Outline each blood parasite and name the species.
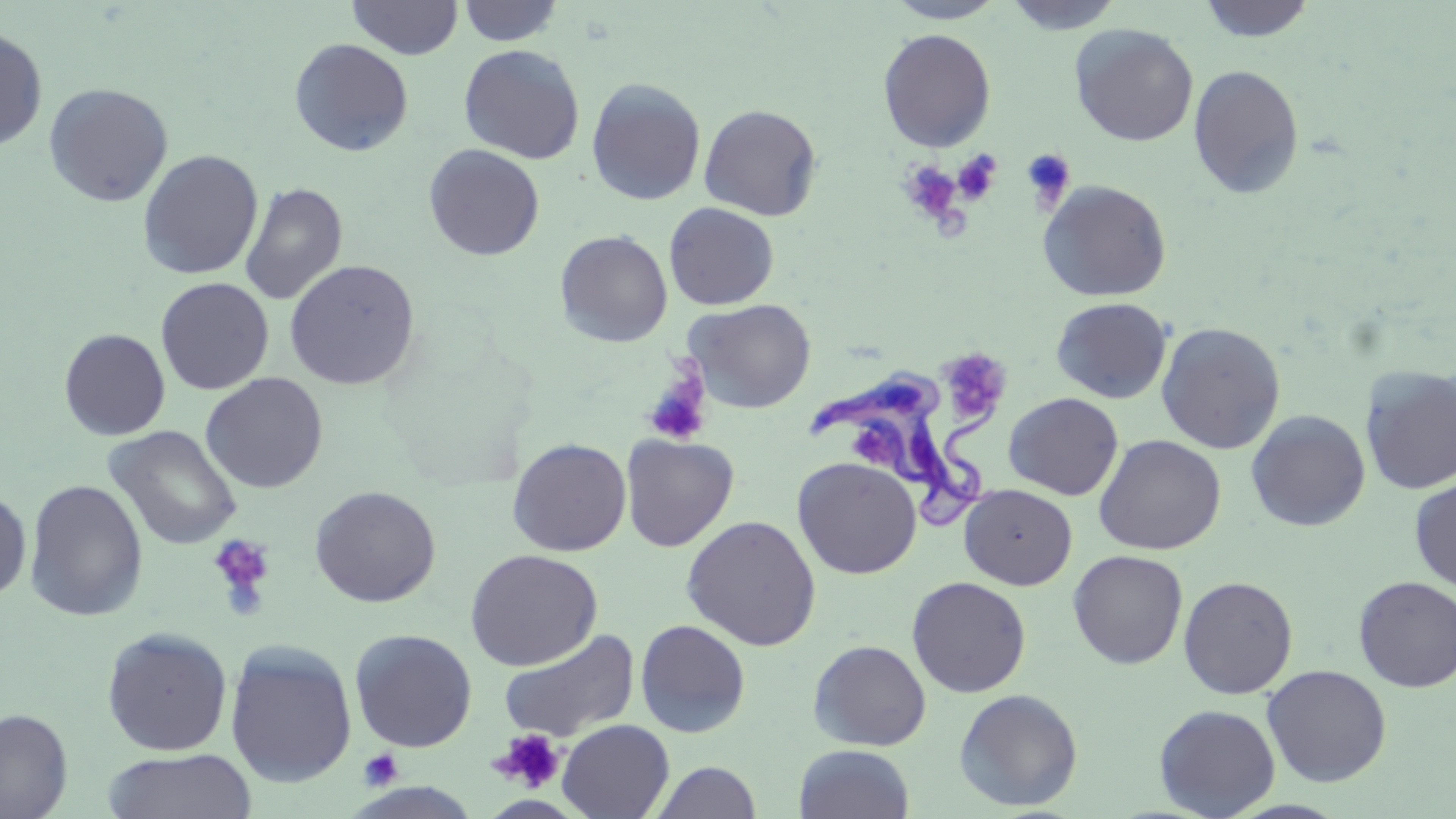

Approximate bounding boxes as [x1, y1, x2, y2] in pixels.
Trypanosoma brucei: [806, 366, 1003, 533].
No Plasmodium falciparum, Plasmodium ovale, Plasmodium malariae, Plasmodium vivax, or Babesia divergens observed.

Uninfected red blood cell locations: [348, 0, 462, 60], [885, 0, 1007, 24], [1002, 0, 1127, 35], [1197, 0, 1316, 42], [457, 1, 563, 46], [1069, 24, 1198, 147], [0, 25, 48, 151], [877, 28, 996, 153], [288, 38, 414, 157], [458, 44, 585, 165], [1188, 64, 1304, 200], [586, 78, 706, 206], [43, 82, 173, 207], [699, 103, 823, 221], [423, 144, 545, 261], [137, 150, 263, 280], [1037, 179, 1172, 302], [240, 182, 348, 306], [663, 203, 779, 310], [554, 230, 673, 347], [283, 259, 420, 390], [155, 277, 274, 395], [1051, 297, 1172, 403], [683, 298, 816, 413], [1155, 321, 1286, 454], [59, 328, 170, 440], [1360, 365, 1456, 495], [200, 373, 328, 494], [1003, 392, 1123, 500], [1245, 409, 1370, 531], [104, 425, 242, 550], [620, 434, 739, 552], [1092, 434, 1226, 555], [507, 437, 631, 557], [792, 457, 922, 579], [1409, 477, 1456, 592], [24, 479, 148, 621], [959, 484, 1077, 590], [309, 485, 441, 607], [0, 490, 32, 602], [682, 514, 821, 651], [464, 549, 602, 671], [1067, 549, 1188, 669], [1178, 575, 1298, 699], [1353, 575, 1456, 693], [906, 576, 1031, 697], [635, 619, 751, 738], [101, 626, 233, 756], [498, 627, 640, 742], [349, 628, 477, 752], [808, 639, 931, 751], [224, 640, 358, 788], [1261, 664, 1391, 787], [953, 688, 1083, 811], [1154, 703, 1281, 818], [0, 708, 73, 819], [557, 719, 674, 819], [794, 744, 915, 819], [102, 749, 257, 819], [650, 761, 762, 819]. Platelet locations: [1019, 148, 1075, 210], [952, 149, 1002, 205], [898, 162, 963, 225], [941, 349, 1016, 423], [641, 369, 712, 446], [852, 429, 896, 468], [208, 534, 275, 612], [493, 729, 565, 793], [359, 749, 403, 790]. Slide-level diagnosis: Trypanosoma brucei. Thin blood film. Optical microscopy. Single field of view. May-Grünwald-Giemsa-stained preparation. Image is 1456×819 pixels. Captured at 1000x magnification.